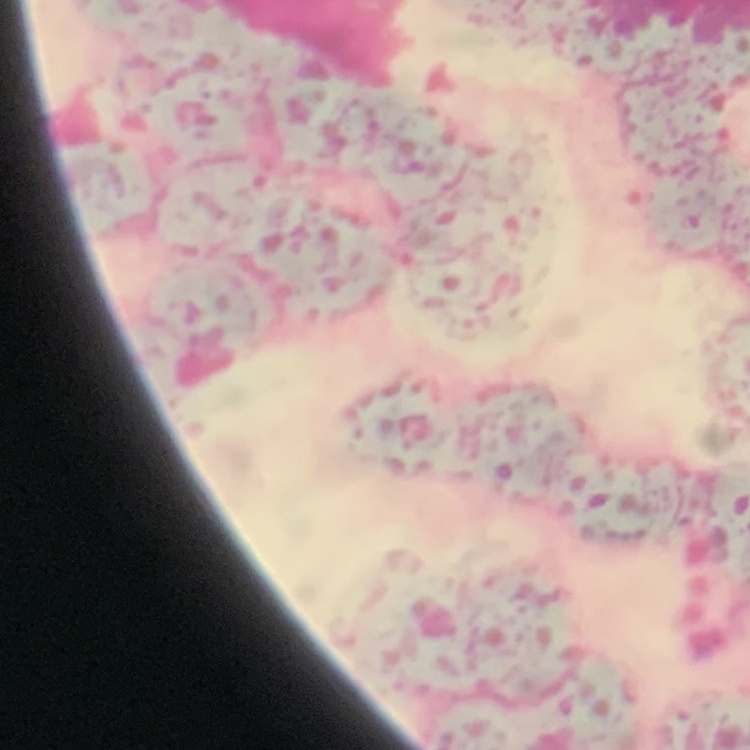

Summary:
  - Erythrocyte morphology: rouleaux formation
  - Stain: Field's or Giemsa
  - Image type: square crop of a larger photomicrograph
  - Preparation: thin peripheral smear